Describe the morphology of the erythrocytes.
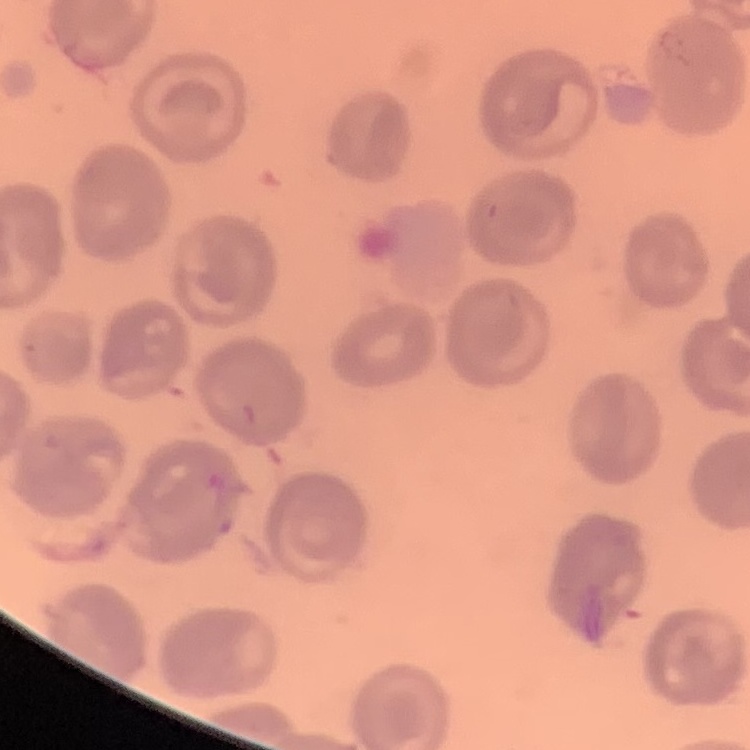

No rouleaux formation.

{
  "stain": "Field's or Giemsa",
  "image_type": "one tile cut from a larger photomicrograph",
  "preparation": "thin peripheral smear"
}